Classify this cell by malaria status.
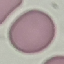

Uninfected.

image_type: cell patch, automatically extracted from a larger field of view and resized to 64 × 64 pixels
stain: Giemsa
preparation: thin blood smear
capture: smartphone camera at the microscope eyepiece